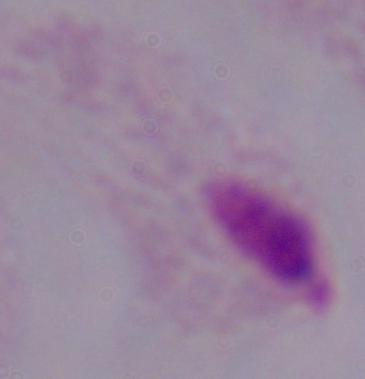

identification = trichomonad
magnification = 1000x
modality = photomicrograph